Report the malaria status of this cell.
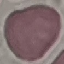
It is uninfected.

Thin blood film. Photographed with a smartphone camera at the microscope eyepiece. Automatically extracted cell patch, resized to 64 × 64 pixels. Giemsa-stained preparation.